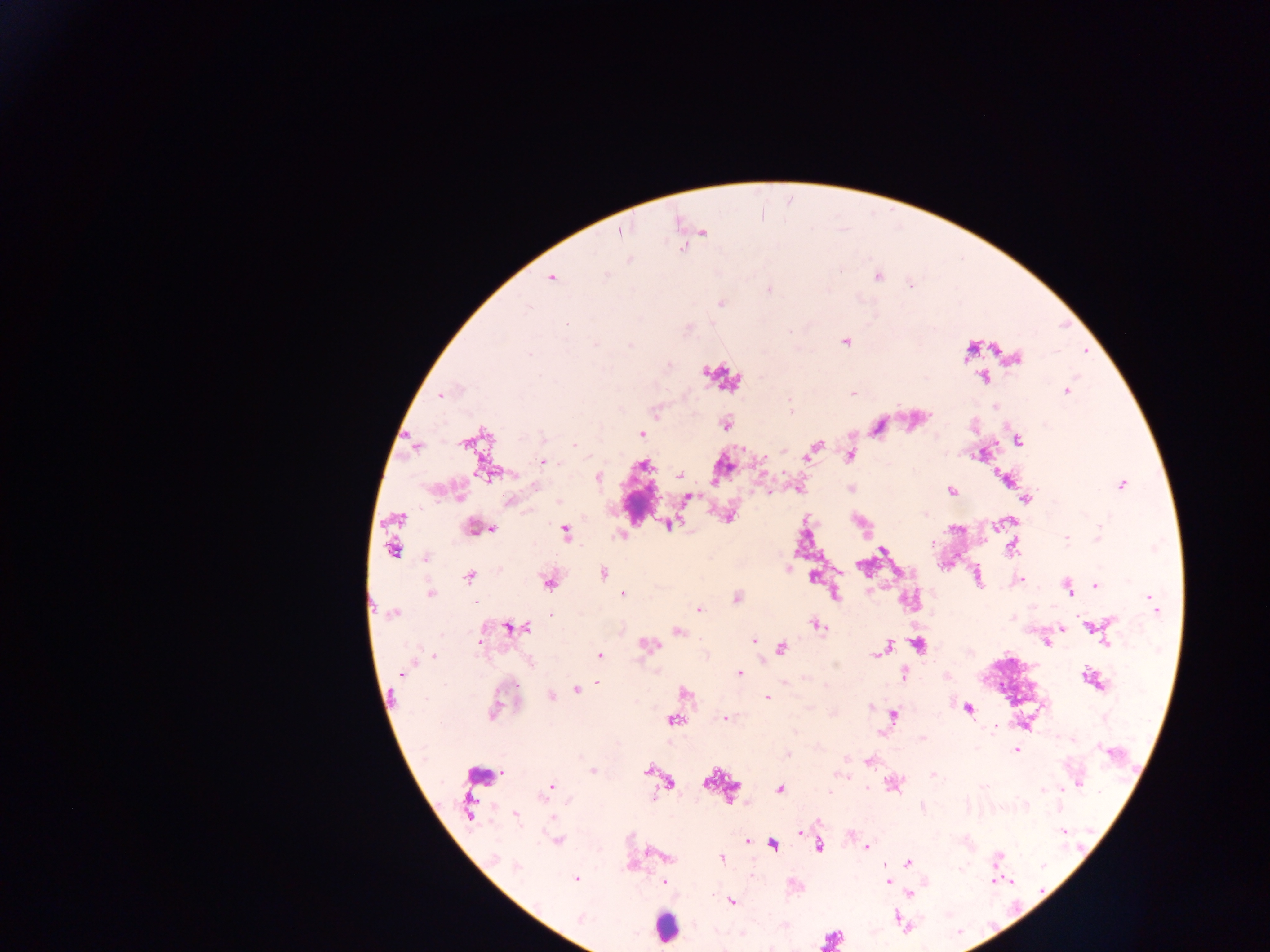

field of view = single
preparation = thick blood smear
capture = mobile-phone photograph through a microscope
image size = 1270×952 pixels
country = Ghana
leukocyte locations = approximate centers as {x, y} in pixels: {721, 377}, {665, 928}
Plasmodium parasite locations = approximate centers as {x, y} in pixels: {619, 231}, {703, 231}, {681, 248}, {630, 260}, {606, 276}, {878, 277}, {552, 278}, {911, 286}, {768, 290}, {721, 303}, {566, 324}, {687, 328}, {845, 341}, {596, 344}, {630, 345}, {530, 354}, {1016, 359}, {983, 378}, {1066, 390}, {853, 394}, {441, 396}, {995, 406}, {791, 411}, {726, 424}, {878, 426}, {641, 433}, {1019, 439}, {465, 442}, {575, 445}, {415, 447}, {814, 448}, {850, 455}, {807, 456}, {544, 462}, {643, 466}, {487, 472}, {680, 476}, {598, 477}, {1122, 484}, {536, 487}, {951, 491}, {767, 492}, {460, 497}, {688, 498}, {1026, 499}, {560, 501}, {510, 502}, {926, 514}, {728, 517}, {396, 519}, {670, 525}, {476, 528}, {493, 529}, {566, 532}, {620, 535}, {1066, 538}, {1098, 539}, {932, 543}, {392, 549}, {882, 549}, {1012, 549}, {426, 557}, {603, 573}, {469, 576}, {813, 577}, {1020, 579}, {549, 583}, {1096, 585}, {1067, 588}, {430, 594}, {623, 594}, {835, 596}, {737, 598}, {1152, 601}, {476, 603}, {699, 609}, {393, 614}, {551, 616}, {818, 626}, {1089, 627}, {511, 628}, {523, 628}, {1061, 628}, {678, 632}, {753, 641}, {480, 642}, {1107, 642}, {1047, 643}, {647, 644}, {918, 645}, {886, 647}, {782, 648}, {881, 651}, {876, 654}, {433, 656}, {600, 656}, {739, 672}, {401, 675}, {903, 676}, {598, 684}, {577, 690}, {685, 692}, {551, 697}, {767, 698}, {870, 707}, {967, 709}, {493, 712}, {894, 715}, {725, 718}, {674, 720}, {995, 729}, {922, 738}, {1104, 750}, {1017, 751}, {787, 754}, {868, 761}, {592, 771}, {647, 771}, {933, 775}, {668, 782}, {1079, 782}, {550, 786}, {983, 786}, {780, 789}, {1043, 789}, {829, 792}, {515, 816}, {800, 832}, {1064, 832}, {557, 841}, {748, 841}, {773, 845}, {819, 847}, {866, 847}, {496, 859}, {722, 859}, {997, 859}, {908, 863}, {517, 867}, {576, 879}, {994, 880}, {888, 881}, {663, 882}, {910, 894}, {731, 901}, {580, 919}, {832, 939}